Point out each Plasmodium parasite.
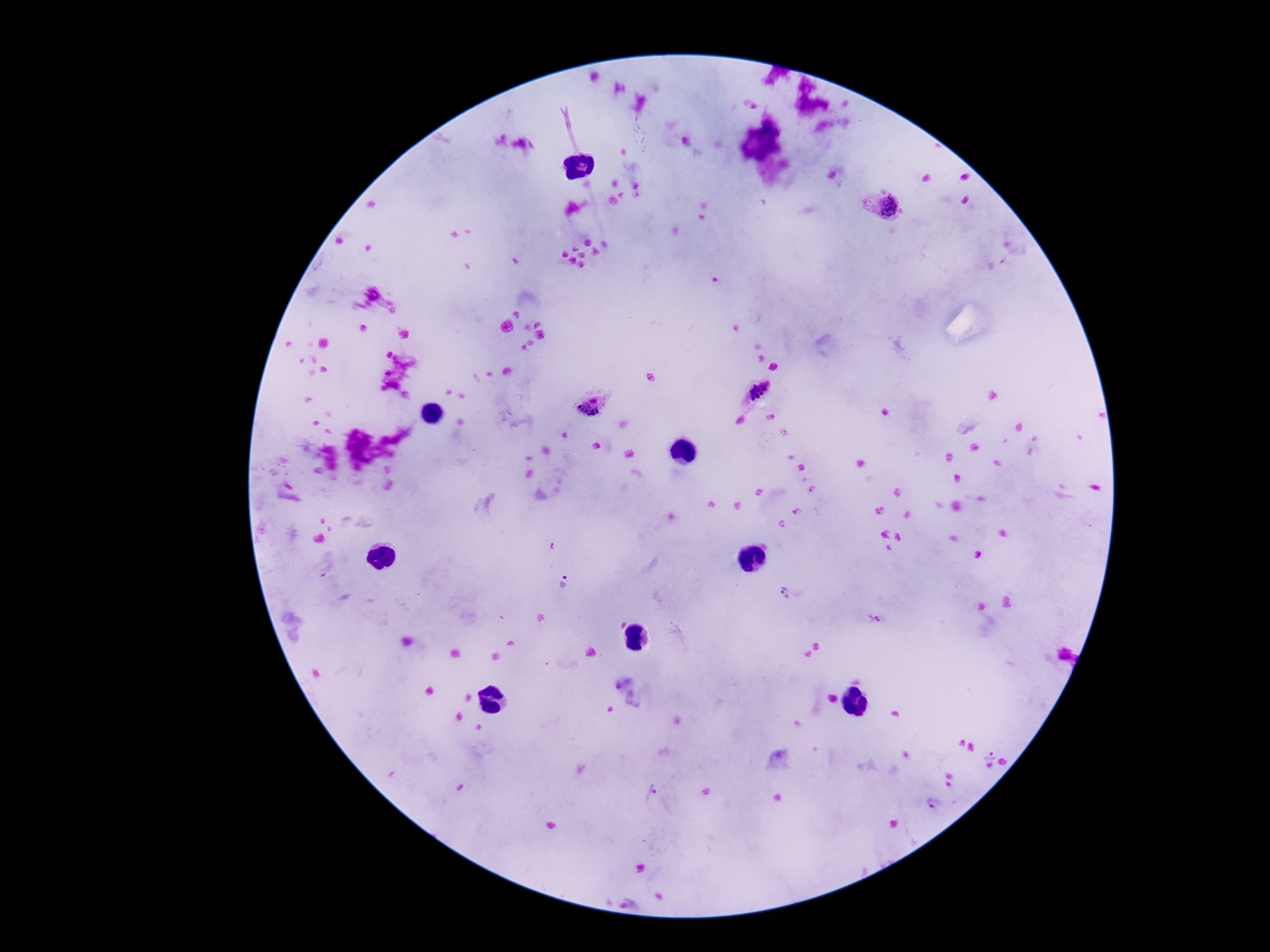
Approximate centers as {x, y} in pixels.
Plasmodium parasites: {687, 144}, {884, 211}, {762, 395}, {595, 406}, {565, 584}, {786, 592}, {875, 619}, {991, 752}, {651, 793}, {934, 803}.

Photographed through the microscope eyepiece with a smartphone camera. Patient malaria status: infected. Giemsa-stained preparation. Image is 1270×952 pixels. Thick blood smear. 100x magnification. One field from this slide.